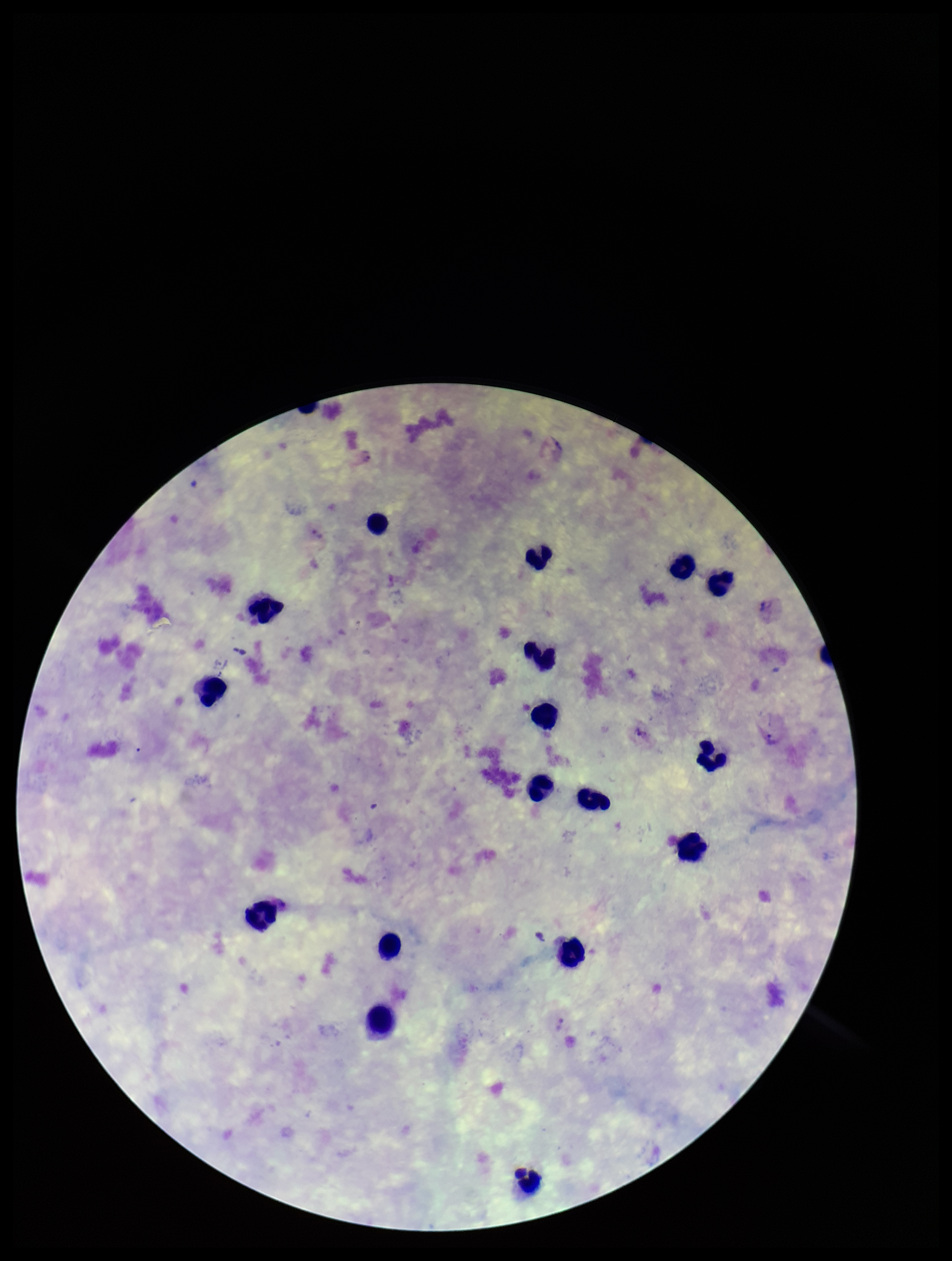
Patient malaria status: positive. Species reported for this patient: Plasmodium vivax. Preparation: thick smear. Leukocyte count: 17. Stained with Giemsa. Photographed through the microscope eyepiece with a smartphone camera. Single field of view. Image is 952×1261 pixels. Plasmodium parasites: identified. Parasite count: 2.